State the blood parasite species.
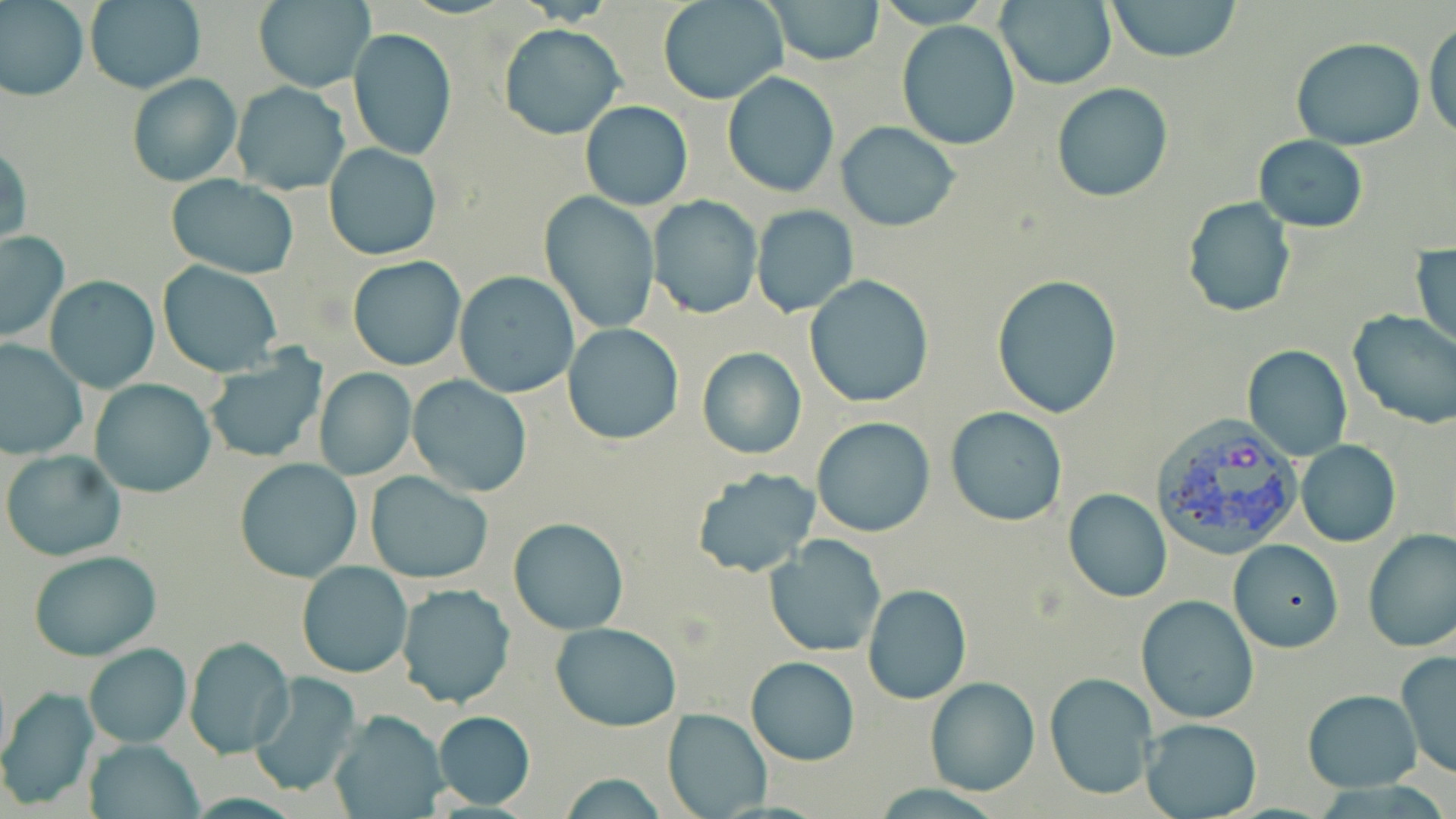
Plasmodium vivax.

Summary:
  - Coordinate format: approximate bounding boxes as (x1,y1)-(x2,y2) corner pairs in pixels
  - Plasmodium vivax-infected red blood cell locations: (1150,416)-(1307,561)
  - Uninfected red blood cell locations: (658,0)-(787,104), (766,0)-(885,65), (995,0)-(1115,89), (1106,0)-(1242,64), (0,1)-(88,101), (84,1)-(204,94), (253,1)-(375,91), (895,20)-(1022,152), (499,23)-(625,139), (1425,23)-(1456,141), (348,28)-(457,161), (1291,37)-(1425,151), (723,72)-(839,197), (127,74)-(241,188), (231,82)-(350,196), (1051,84)-(1175,202), (580,101)-(692,210), (836,122)-(961,231), (1253,134)-(1369,233), (0,143)-(31,251), (323,143)-(444,261), (166,176)-(298,278), (541,193)-(659,334), (648,195)-(761,319), (1181,196)-(1297,319), (750,204)-(858,318), (0,230)-(70,343), (1412,242)-(1456,348), (347,255)-(466,370), (158,261)-(282,377), (453,270)-(581,397), (992,274)-(1123,417), (804,276)-(934,407), (45,277)-(158,392), (1347,310)-(1456,429), (563,323)-(685,445), (0,339)-(89,460), (4,341)-(102,563), (1243,344)-(1352,462), (697,346)-(806,460), (203,352)-(328,464), (313,367)-(416,481), (407,375)-(532,498), (89,378)-(216,498), (945,407)-(1069,527), (810,417)-(935,538), (1297,440)-(1401,548), (1,450)-(127,561), (234,458)-(362,582), (691,468)-(820,579), (365,472)-(493,585), (1063,488)-(1172,603), (508,517)-(629,634), (1361,528)-(1456,653), (766,536)-(886,659), (1229,540)-(1343,653), (28,550)-(162,661), (296,560)-(412,678), (862,583)-(970,703), (397,584)-(513,709), (1134,595)-(1258,725), (550,622)-(682,732), (185,636)-(293,758), (82,644)-(191,748), (1395,650)-(1456,779), (746,656)-(858,766), (249,672)-(363,797), (1045,672)-(1157,800), (923,674)-(1041,797), (1,688)-(100,808), (1303,689)-(1422,792), (662,706)-(772,819), (327,710)-(449,817), (432,711)-(535,809), (1138,718)-(1263,819), (81,738)-(205,819), (552,771)-(671,818)
  - Field of view: single
  - Image size: 1456×819 pixels
  - Modality: light microscopy
  - Preparation: thin blood film
  - Magnification: 1000x
  - Stain: May-Grünwald-Giemsa